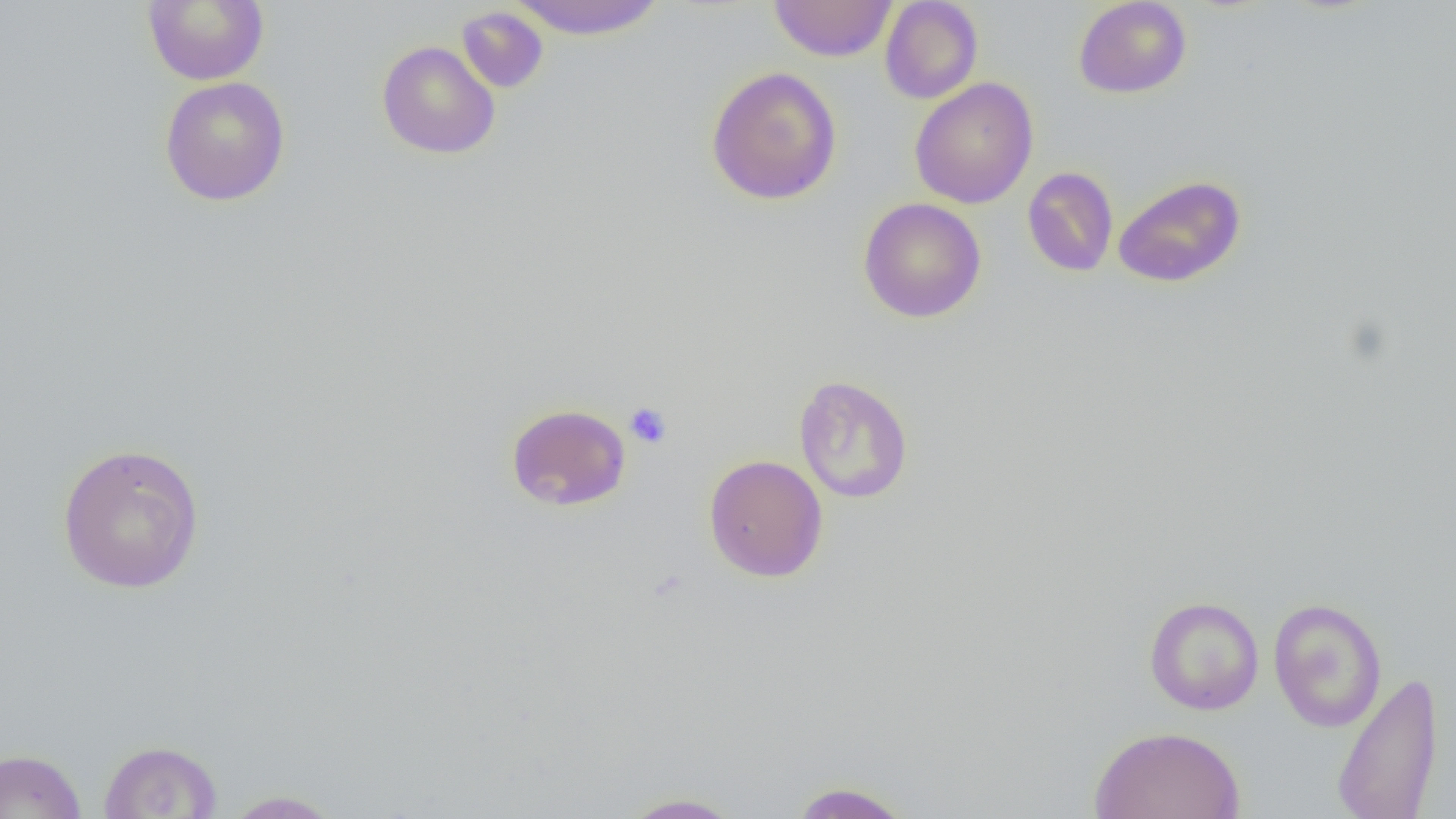

slide-level diagnosis = no evidence of blood parasites
field of view = single
preparation = thin blood smear
uninfected red blood cell locations = approximate bounding boxes as [x1, y1, x2, y2] in pixels: [142, 0, 269, 86], [506, 0, 669, 40], [770, 0, 897, 62], [1073, 0, 1193, 99], [879, 1, 983, 103], [456, 6, 548, 94], [376, 40, 500, 159], [705, 66, 842, 205], [159, 76, 291, 206], [909, 77, 1039, 209], [1022, 166, 1119, 277], [1113, 175, 1246, 287], [859, 197, 986, 323], [794, 374, 913, 503], [505, 403, 631, 511], [56, 442, 206, 595], [703, 454, 828, 582], [1143, 596, 1264, 715], [1268, 597, 1387, 732], [1332, 670, 1444, 819], [1088, 725, 1246, 819], [98, 740, 223, 818], [0, 748, 88, 819], [787, 781, 916, 819], [218, 789, 347, 818], [617, 792, 746, 818]
platelet locations = approximate bounding boxes as [x1, y1, x2, y2] in pixels: [624, 402, 673, 450]
modality = light microscopy
image size = 1456×819 pixels
magnification = 1000x